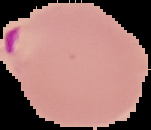
image type = segmented cell region with the area outside set to black
preparation = thin blood smear
image size = 151×130 pixels
result = malaria parasites detected